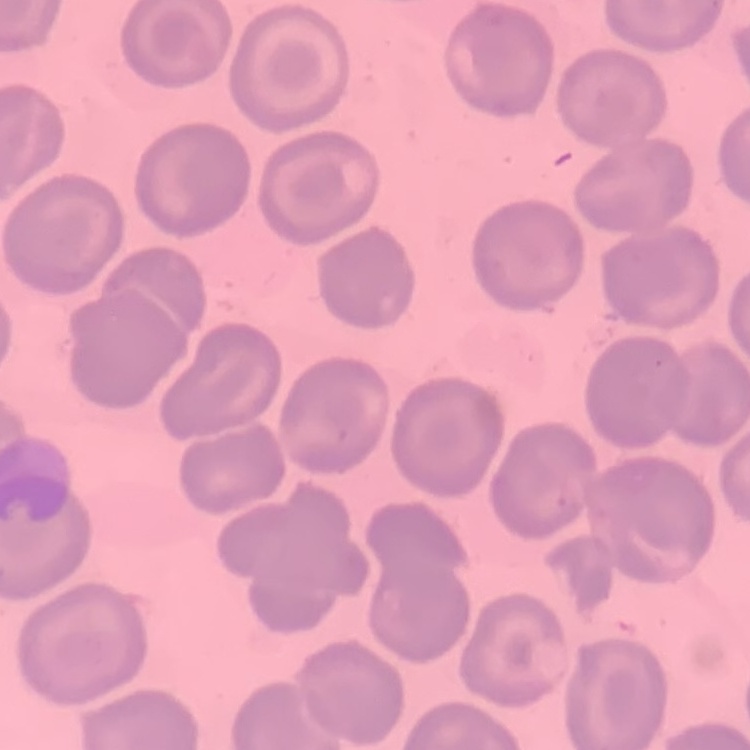

{
  "erythrocyte_morphology": "no rouleaux formation",
  "stain": "Field's or Giemsa",
  "preparation": "thin peripheral smear",
  "image_type": "one tile cut from a larger photomicrograph"
}